Classify this cell by malaria status.
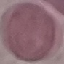

Uninfected.

Summary:
  - Image type: automatically extracted cell patch, resized to 64 × 64 pixels
  - Preparation: thin blood film
  - Stain: Giemsa
  - Capture: smartphone camera at the microscope eyepiece